Locate every malaria parasite.
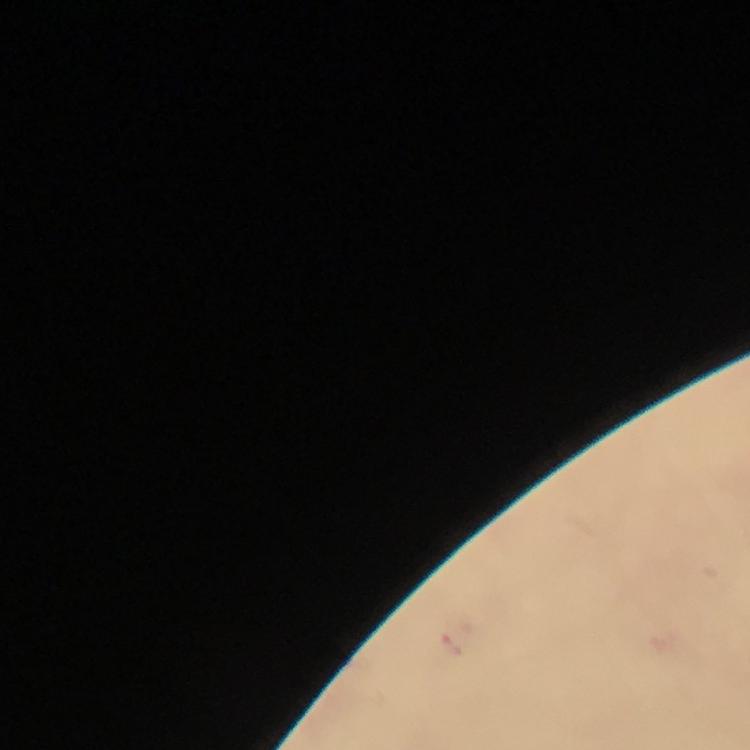

Approximate centers as [x, y] in pixels.
Malaria parasites: [457, 641].

immersion_oil: applied
preparation: thick blood film
cropped_from: a single field of view
capture: smartphone photograph through a microscope
magnification: 100x
stain: Giemsa
context: from a malaria diagnostic workup
image_size: 750×750 pixels